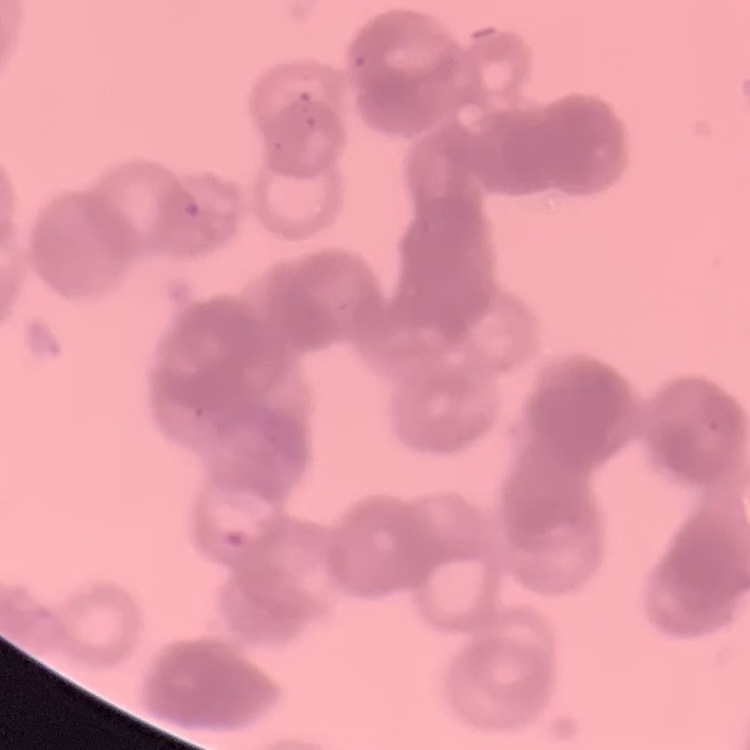

red blood cell morphology = rouleaux formation
preparation = thin blood smear
image type = square crop of a larger photomicrograph
stain = Field's or Giemsa